Assess this cell for malaria.
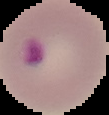

Parasitized.

image_size: 109×115 pixels
preparation: thin blood film
image_type: segmented cell region with the area outside set to black